State the blood parasite species.
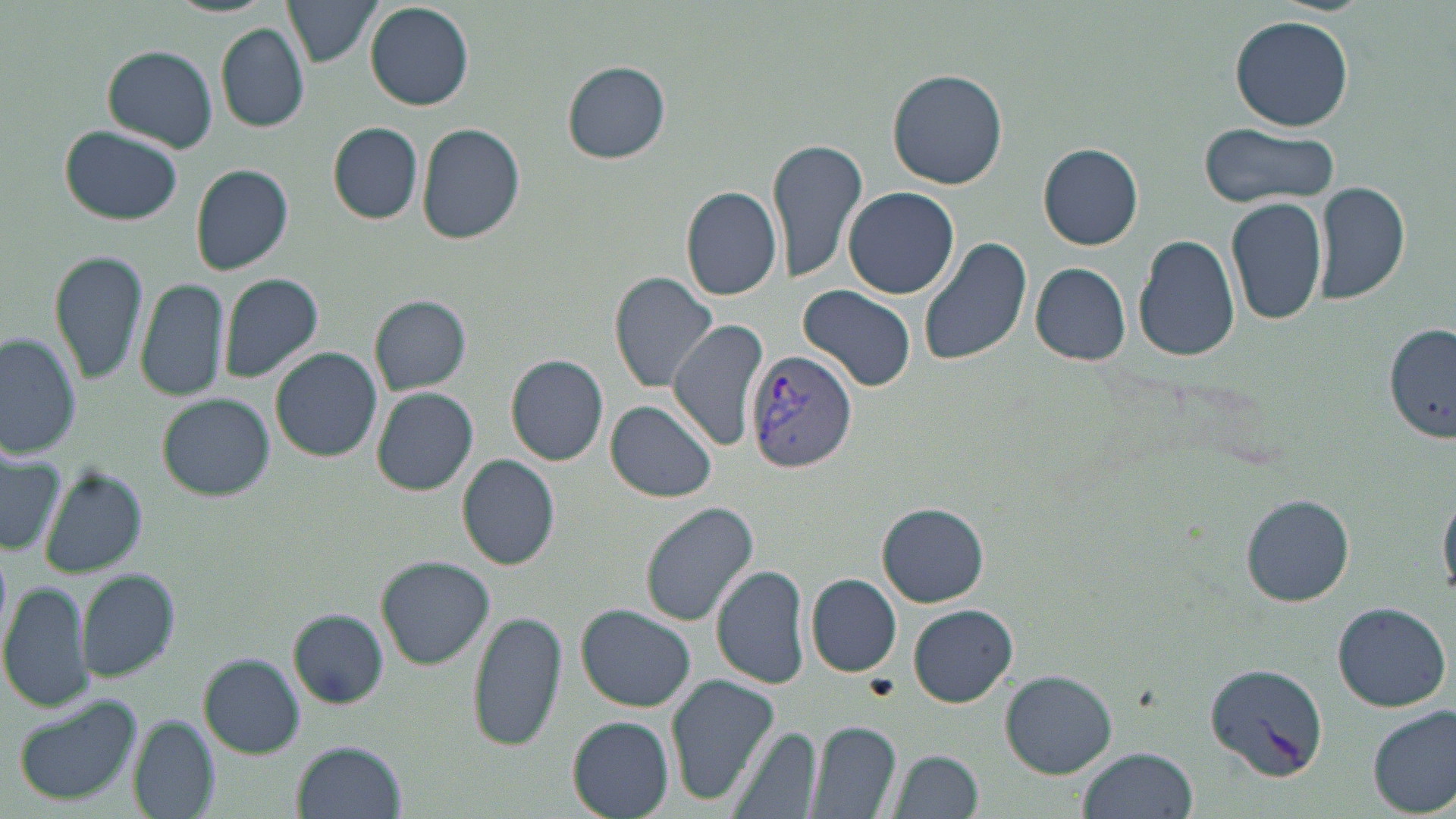

Plasmodium vivax.

modality = light microscopy
uninfected red blood cell locations = approximate bounding boxes as (x1, y1, x2, y2) in pixels: (286, 0, 382, 67), (366, 3, 474, 112), (1230, 14, 1355, 131), (216, 23, 310, 131), (102, 44, 218, 152), (563, 62, 669, 163), (887, 69, 1010, 190), (329, 122, 424, 224), (416, 122, 524, 245), (1198, 122, 1341, 208), (62, 126, 183, 224), (768, 136, 870, 285), (1039, 143, 1145, 250), (191, 163, 295, 276), (1313, 179, 1411, 306), (681, 185, 783, 300), (844, 186, 959, 299), (1226, 196, 1329, 325), (1134, 234, 1242, 362), (918, 236, 1033, 367), (49, 248, 148, 385), (1030, 261, 1131, 366), (220, 272, 325, 384), (610, 272, 720, 392), (134, 277, 231, 402), (799, 287, 916, 391), (371, 296, 470, 395), (665, 321, 769, 450), (1387, 324, 1455, 443), (0, 332, 81, 461), (270, 347, 382, 462), (507, 355, 608, 465), (371, 388, 478, 497), (156, 394, 277, 498), (606, 402, 717, 501), (0, 448, 65, 556), (457, 454, 563, 570), (39, 468, 146, 578), (1439, 482, 1456, 601), (1241, 495, 1355, 606), (639, 502, 759, 626), (878, 505, 988, 607), (377, 556, 494, 669), (712, 563, 810, 690), (78, 571, 179, 684), (806, 575, 902, 676), (1, 578, 95, 713), (1331, 601, 1451, 712), (908, 604, 1018, 708), (577, 606, 696, 712), (468, 607, 567, 752), (288, 609, 389, 708), (200, 655, 303, 757), (1002, 670, 1116, 777), (664, 671, 781, 805), (10, 693, 144, 808), (1369, 707, 1455, 816), (568, 715, 676, 818), (129, 718, 219, 818), (809, 721, 901, 818), (731, 726, 822, 819), (293, 740, 406, 819), (1077, 748, 1197, 819), (889, 750, 983, 819)
stain = May-Grünwald-Giemsa
field of view = one of a larger specimen
magnification = 1000x
preparation = thin blood film
Plasmodium vivax-infected red blood cell locations = approximate bounding boxes as (x1, y1, x2, y2) in pixels: (743, 348, 859, 475), (1204, 662, 1328, 783)
image size = 1456×819 pixels